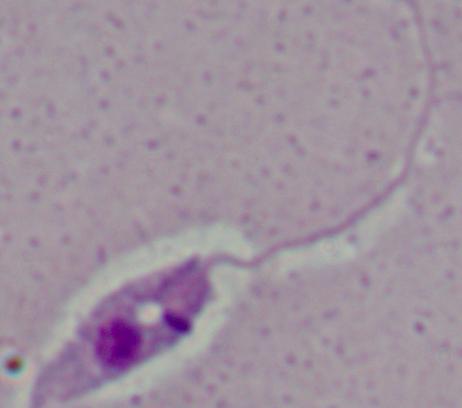

magnification = 1000x
identification = Leishmania
modality = photomicrograph